Locate and identify every blood parasite.
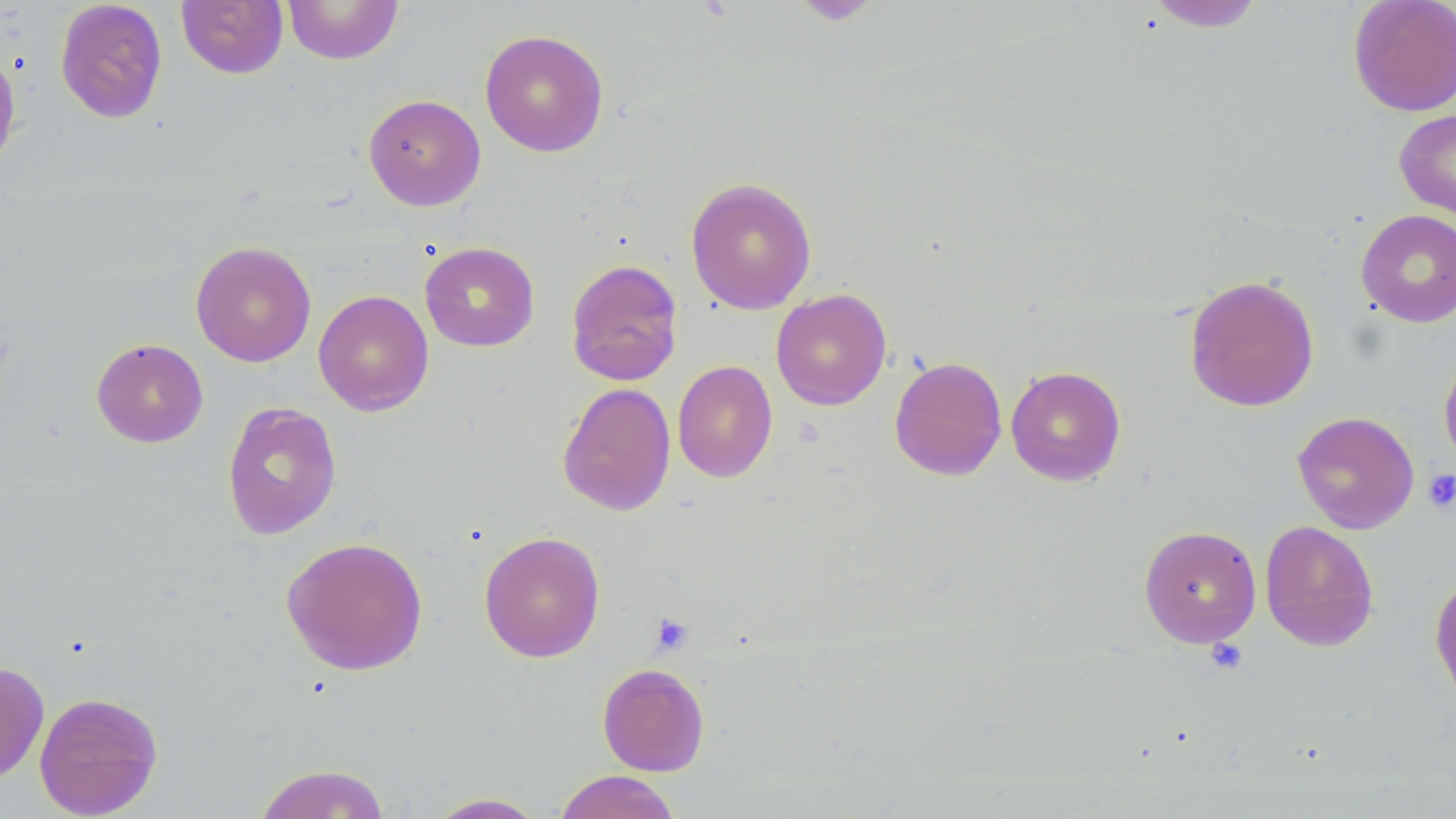

No blood parasites seen.

Summary:
  - Coordinate format: approximate bounding boxes as named x1/y1/x2/y2 corners in pixels
  - Platelet locations (subset): (x1=1423, y1=469, x2=1456, y2=513), (x1=650, y1=613, x2=693, y2=654), (x1=1205, y1=638, x2=1248, y2=675)
  - Uninfected red blood cell locations (subset): (x1=55, y1=0, x2=168, y2=123), (x1=177, y1=0, x2=288, y2=79), (x1=283, y1=0, x2=402, y2=65), (x1=1347, y1=0, x2=1456, y2=117), (x1=1144, y1=1, x2=1266, y2=32), (x1=479, y1=28, x2=609, y2=157), (x1=0, y1=47, x2=22, y2=172), (x1=363, y1=93, x2=486, y2=211), (x1=1394, y1=109, x2=1456, y2=224), (x1=685, y1=177, x2=817, y2=314), (x1=1356, y1=209, x2=1456, y2=328), (x1=190, y1=241, x2=316, y2=367), (x1=419, y1=241, x2=540, y2=352), (x1=566, y1=258, x2=684, y2=386), (x1=1184, y1=274, x2=1320, y2=412), (x1=770, y1=288, x2=892, y2=410), (x1=313, y1=289, x2=434, y2=416), (x1=91, y1=338, x2=208, y2=448), (x1=1438, y1=351, x2=1456, y2=472), (x1=889, y1=356, x2=1008, y2=481), (x1=672, y1=360, x2=777, y2=482), (x1=1005, y1=365, x2=1127, y2=486), (x1=557, y1=382, x2=676, y2=516), (x1=221, y1=401, x2=342, y2=541), (x1=1292, y1=411, x2=1420, y2=534), (x1=1259, y1=520, x2=1380, y2=652), (x1=1138, y1=524, x2=1262, y2=648), (x1=478, y1=531, x2=605, y2=662), (x1=280, y1=536, x2=428, y2=675), (x1=1430, y1=572, x2=1456, y2=710), (x1=0, y1=661, x2=49, y2=785), (x1=597, y1=662, x2=710, y2=776), (x1=34, y1=691, x2=163, y2=818), (x1=253, y1=763, x2=392, y2=819), (x1=553, y1=770, x2=682, y2=819), (x1=425, y1=792, x2=549, y2=818)
  - Slide-level diagnosis: negative for blood parasites
  - Field of view: one of a larger specimen
  - Image size: 1456×819 pixels
  - Modality: light microscopy
  - Preparation: thin blood film
  - Stain: May-Grünwald-Giemsa
  - Magnification: 1000x